Identify the parasite.
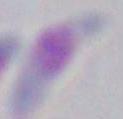

This is Toxoplasma gondii.

Summary:
  - Magnification: 1000x
  - Modality: micrograph